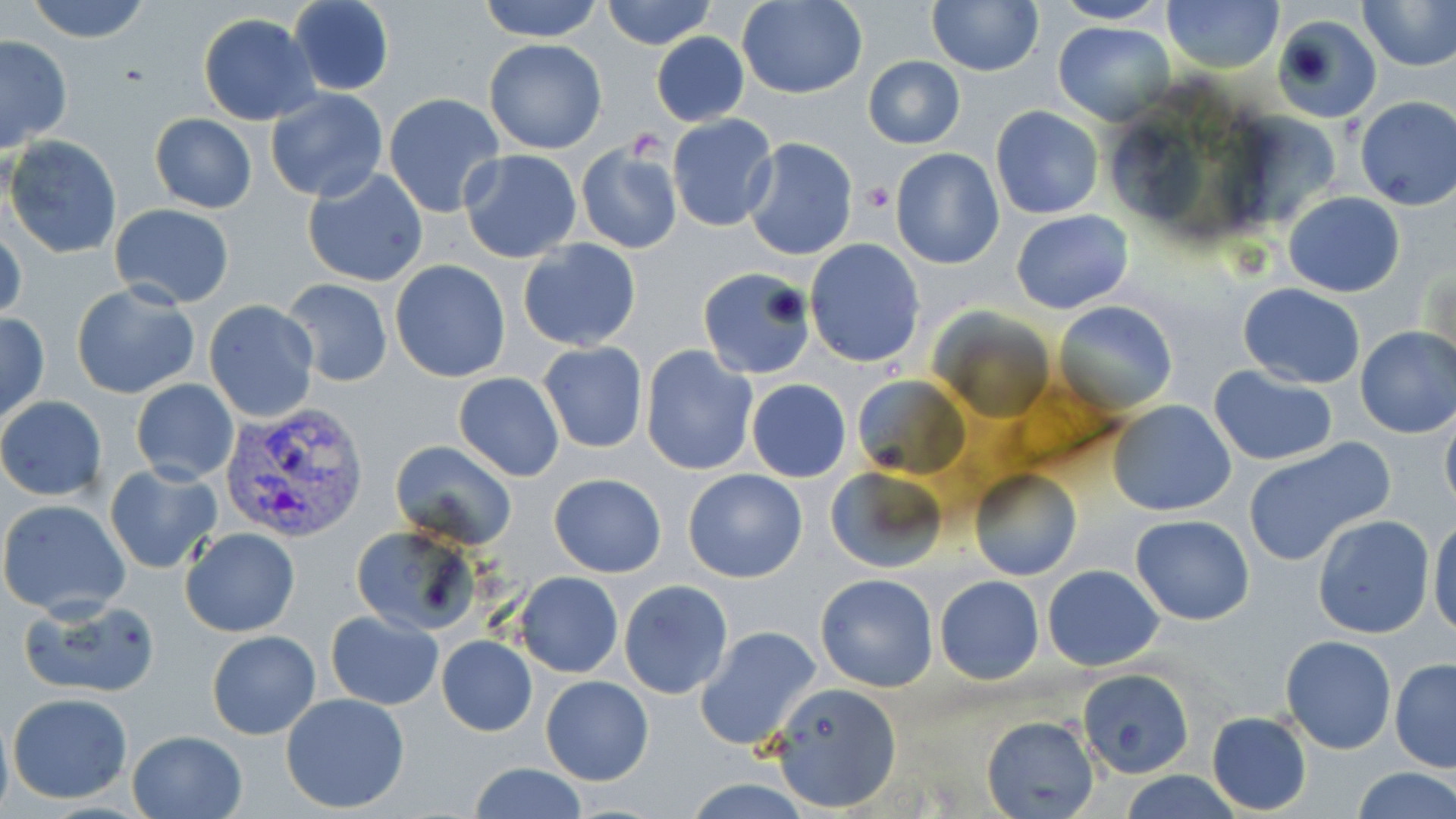

Approximate bounding boxes as (x1, y1, x2, y2) in pixels. Plasmodium vivax-infected red blood cell locations: (220, 402, 370, 545). Platelet locations: (862, 180, 894, 212). Uninfected red blood cell locations: (24, 0, 155, 44), (477, 0, 605, 41), (602, 0, 716, 48), (738, 0, 867, 98), (927, 0, 1042, 74), (1162, 0, 1284, 73), (1359, 0, 1456, 71), (286, 1, 396, 95), (1053, 1, 1170, 24), (198, 13, 319, 125), (1274, 15, 1378, 122), (1054, 20, 1176, 126), (650, 33, 749, 126), (0, 35, 73, 152), (483, 38, 608, 154), (208, 55, 348, 177), (863, 55, 965, 149), (264, 88, 388, 203), (383, 93, 505, 217), (1354, 96, 1456, 210), (991, 105, 1103, 220), (136, 110, 248, 304), (150, 113, 256, 213), (667, 114, 778, 233), (6, 136, 123, 259), (742, 137, 858, 260), (574, 140, 684, 255), (890, 148, 1005, 269), (458, 149, 583, 262), (301, 166, 427, 286), (1283, 191, 1406, 297), (109, 203, 234, 309), (1010, 210, 1133, 314), (1, 218, 26, 326), (517, 238, 641, 352), (804, 238, 925, 368), (1420, 255, 1455, 374), (390, 260, 510, 383), (698, 269, 812, 380), (282, 278, 394, 386), (71, 282, 199, 399), (1238, 284, 1366, 387), (204, 299, 320, 423), (1054, 301, 1177, 411), (933, 308, 1055, 419), (0, 311, 49, 426), (1354, 326, 1456, 438), (538, 340, 648, 453), (641, 345, 760, 477), (1209, 365, 1339, 466), (852, 372, 970, 480), (454, 373, 565, 482), (131, 379, 239, 484), (747, 379, 850, 482), (0, 396, 107, 500), (1108, 399, 1236, 517), (1440, 405, 1456, 520), (1242, 438, 1392, 566), (390, 440, 517, 551), (105, 463, 222, 573), (825, 465, 949, 576), (683, 468, 809, 583), (968, 470, 1081, 582), (549, 473, 667, 577), (0, 498, 131, 618), (1131, 515, 1255, 624), (1311, 515, 1436, 639), (1429, 517, 1456, 638), (351, 525, 480, 634), (180, 528, 300, 637), (1043, 564, 1165, 671), (514, 573, 624, 678), (816, 573, 939, 692), (934, 575, 1044, 684), (619, 580, 731, 700), (18, 596, 160, 700), (325, 610, 443, 710), (695, 625, 823, 752), (207, 630, 321, 739), (1279, 634, 1397, 754), (438, 636, 537, 737), (1389, 657, 1456, 772), (1078, 670, 1193, 778), (541, 675, 654, 785), (768, 681, 901, 812), (7, 692, 134, 805), (282, 692, 410, 814), (0, 711, 13, 819), (1206, 712, 1312, 814), (982, 716, 1100, 819), (126, 730, 248, 819), (466, 762, 588, 819), (1351, 768, 1456, 819), (1121, 771, 1243, 818), (681, 777, 817, 817). Slide-level diagnosis: Plasmodium vivax. Single field of view. Image is 1456×819 pixels. Light microscopy. Captured at 1000x magnification. May-Grünwald-Giemsa-stained preparation. Thin blood film.